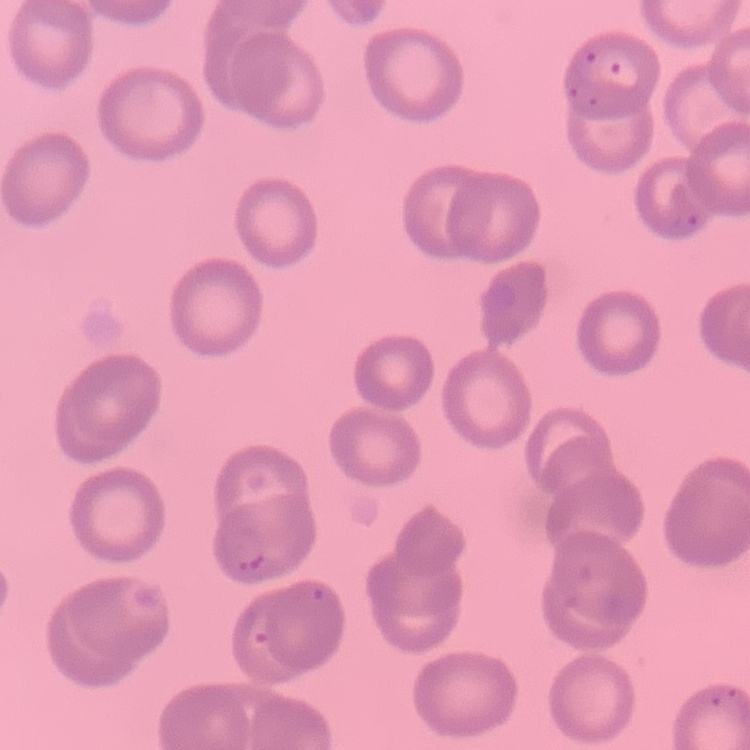
Summary:
  - Erythrocyte morphology: no rouleaux formation
  - Image type: one tile cut from a larger photomicrograph
  - Stain: Field's or Giemsa
  - Preparation: thin peripheral smear